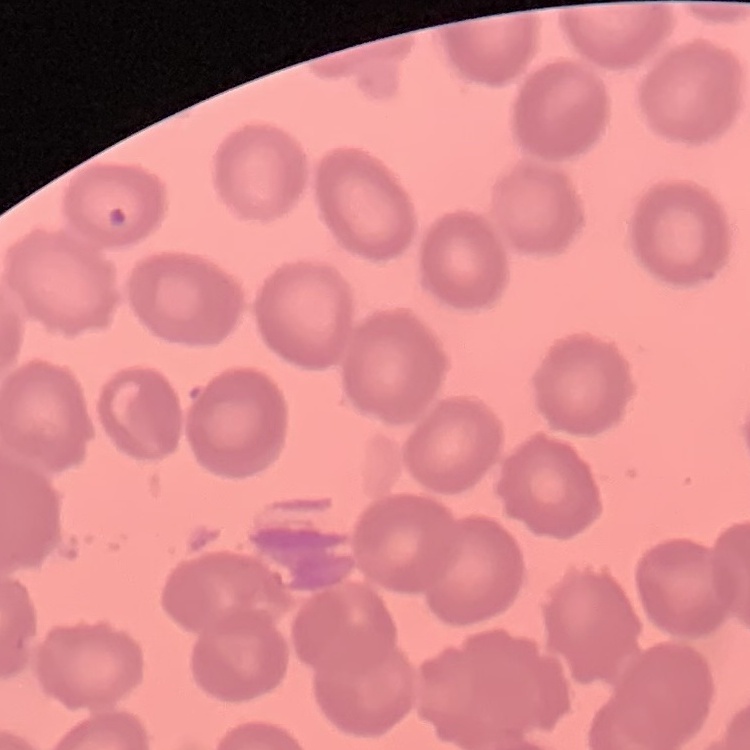
{
  "red_blood_cell_morphology": "no rouleaux formation",
  "stain": "Field's or Giemsa",
  "preparation": "thin peripheral smear",
  "image_type": "square crop of a larger photomicrograph"
}